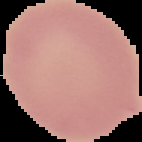
Malaria status: uninfected. The area outside the segmented cell region is set to black. From a thin blood smear. Image is 142×142 pixels.